Report the malaria status of this cell.
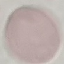

Uninfected.

Acquired by smartphone through the microscope eyepiece. Giemsa-stained preparation. Thin blood smear. Automatically extracted cell patch, resized to 64 × 64 pixels.